Assess the morphology of the red blood cells.
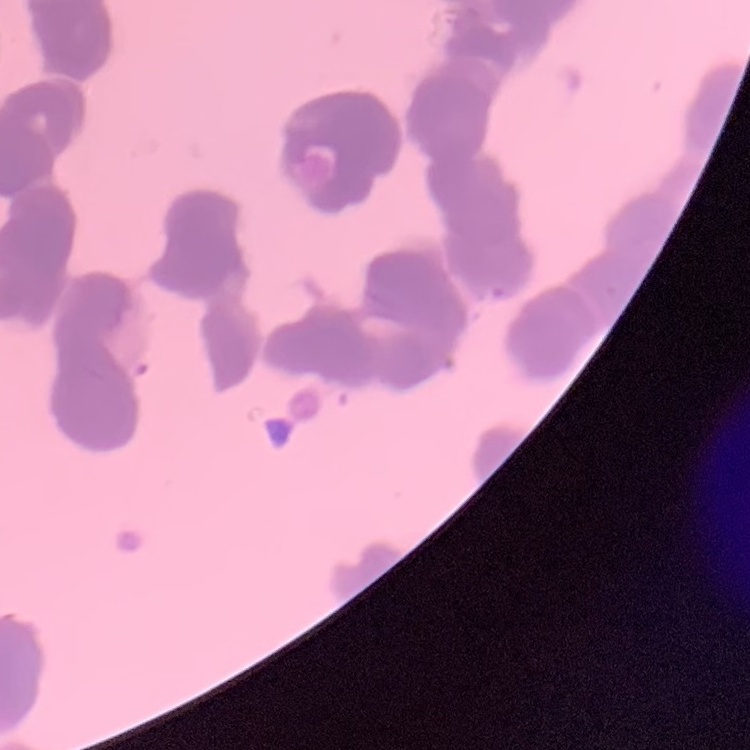

Rouleaux formation.

{
  "preparation": "thin blood smear",
  "image_type": "one tile cut from a larger photomicrograph",
  "stain": "Field's or Giemsa"
}